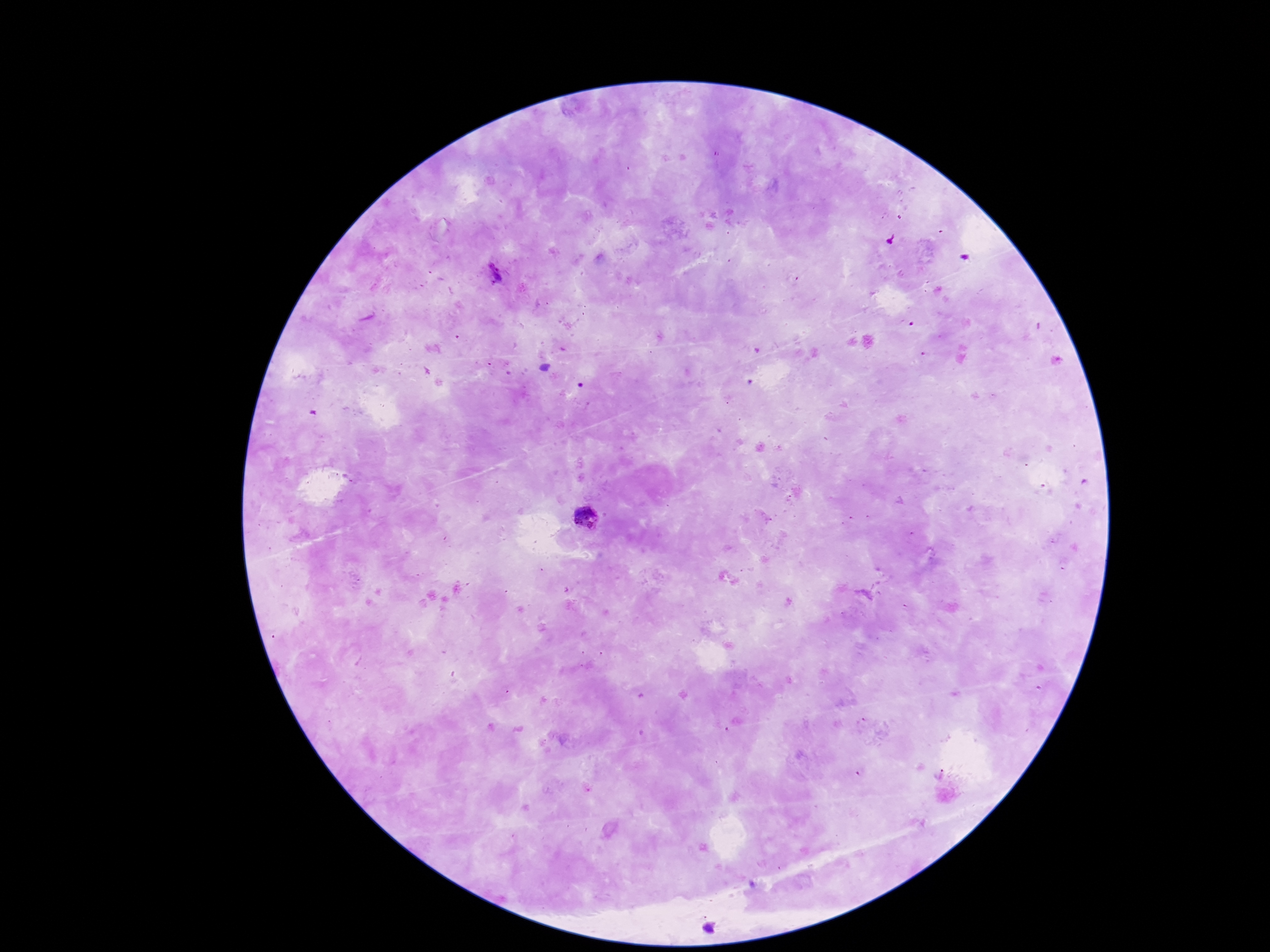
stain = Giemsa
field of view = one from this slide
image size = 1270×952 pixels
capture = smartphone camera through the microscope eyepiece
patient malaria status = positive
Plasmodium parasite locations = approximate centers as (x, y) in pixels: (495, 276), (589, 519)
magnification = 100x
preparation = thick blood film